Assess this cell for malaria.
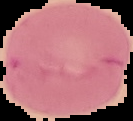
Uninfected.

From a thin blood film. Cell region segmented out of the field of view; the surrounding area is masked to black. Image is 133×121 pixels.